Classify this cell by malaria status.
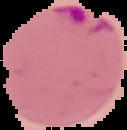

It is parasitized.

From a thin blood film. Image is 127×130 pixels. The area outside the segmented cell region is set to black.